Locate every Plasmodium parasite and every leukocyte.
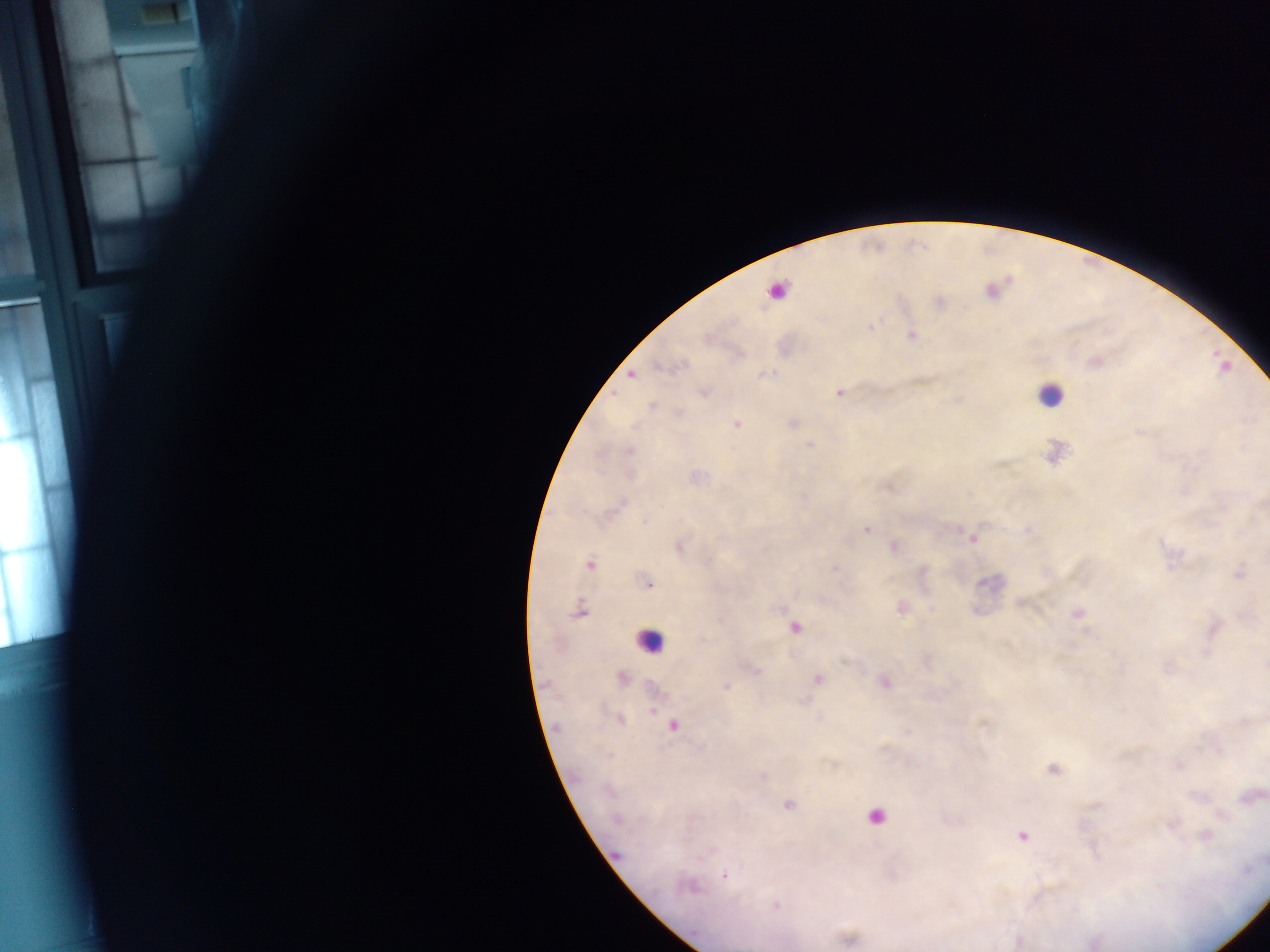

Approximate centers as (x, y) in pixels.
Plasmodium parasites: (776, 291), (911, 335), (632, 374), (704, 392), (839, 392), (652, 406), (736, 424), (810, 445), (629, 452), (866, 530), (972, 538), (679, 546), (894, 547), (589, 563), (835, 568), (1239, 574), (648, 585), (579, 612), (1080, 613), (795, 627), (754, 669), (621, 677), (818, 679), (885, 683), (727, 687), (654, 712), (621, 720), (673, 725), (1053, 769), (763, 777), (1250, 797), (789, 805), (616, 819), (1021, 836), (1205, 836), (725, 876), (692, 888), (776, 905).
Leukocytes: (1050, 395), (649, 640), (873, 817).

preparation = thick blood film
field of view = single
country = Ghana
image size = 1270×952 pixels
capture = mobile-phone photograph through a microscope